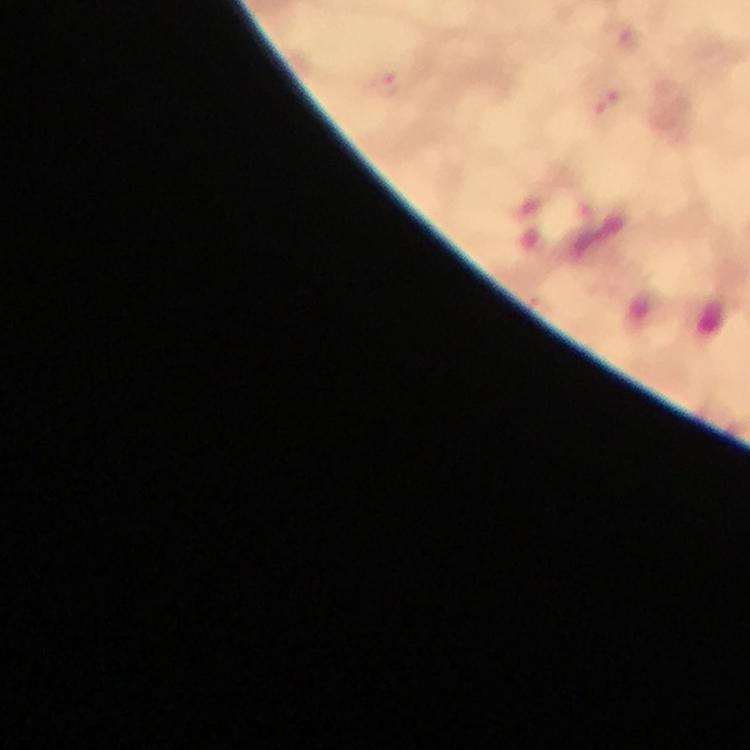

{
  "stain": "Giemsa",
  "malaria_parasite_locations": "approximate centers as [x, y] in pixels: [388, 87]",
  "immersion_oil": "used",
  "capture": "smartphone camera through the microscope",
  "cropped_from": "a single field of view",
  "context": "from a diagnostic examination for malaria",
  "image_size": "750×750 pixels",
  "magnification": "100x",
  "preparation": "thick blood smear"
}